Draw a bounding box around every leukocyte (white blood cell).
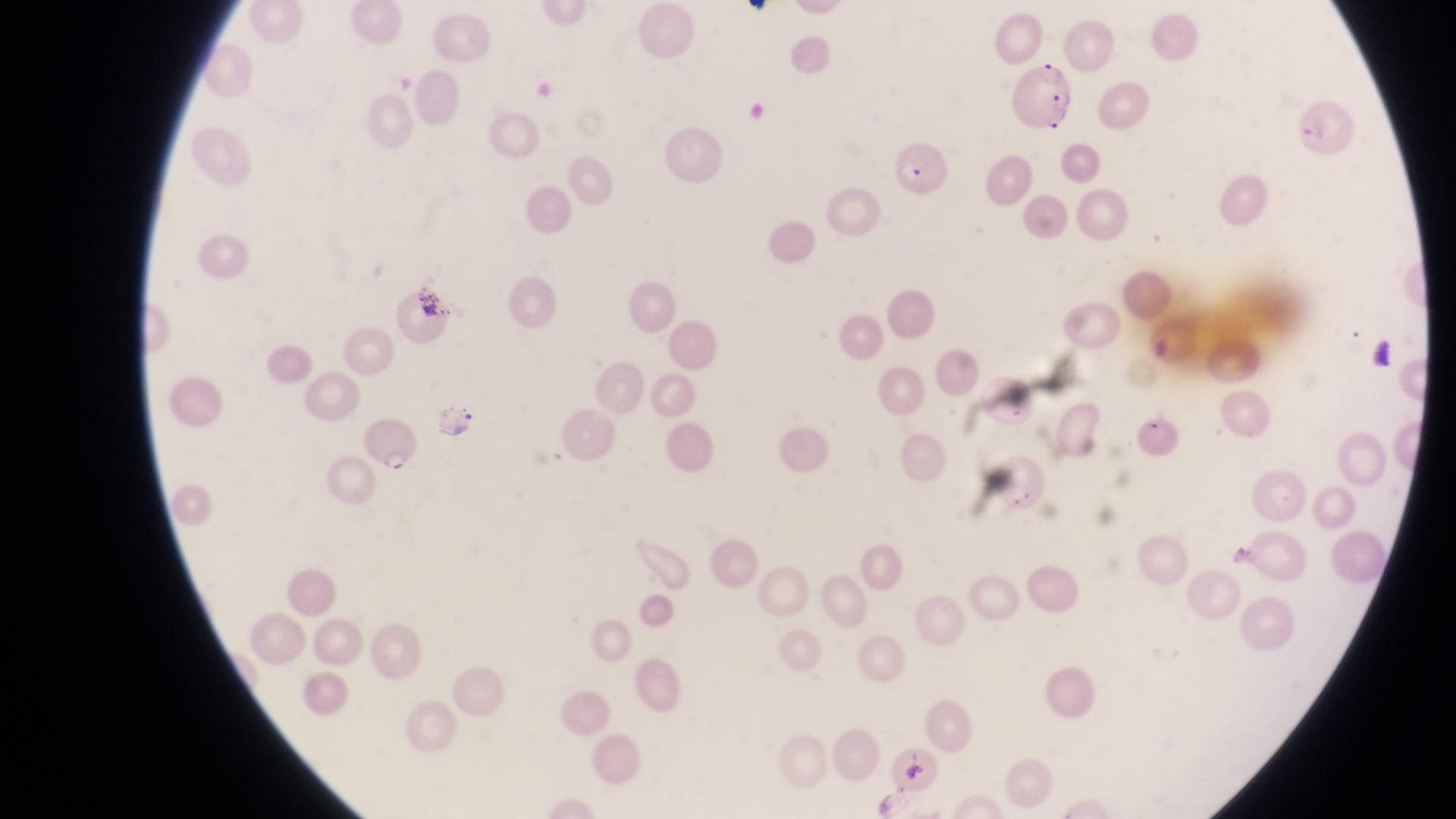
No leukocytes observed.

Approximate bounding boxes as left top right bottom in pixels. Artifact (platelet-like body, stain precipitate, or debris) locations: 407 284 452 320. Parasitised red blood cell locations: 1007 58 1076 131; 1294 92 1360 156; 893 136 952 200; 362 415 420 478; 984 444 1050 515. Image is 1456×819 pixels. Thin blood film. Magnification of 1000x. One field of view. Captured by a smartphone held over the eyepiece of an Olympus CX-23 microscope. Collected in Uganda.